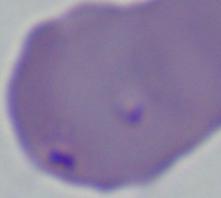

identification = Babesia
magnification = 1000x
modality = photomicrograph